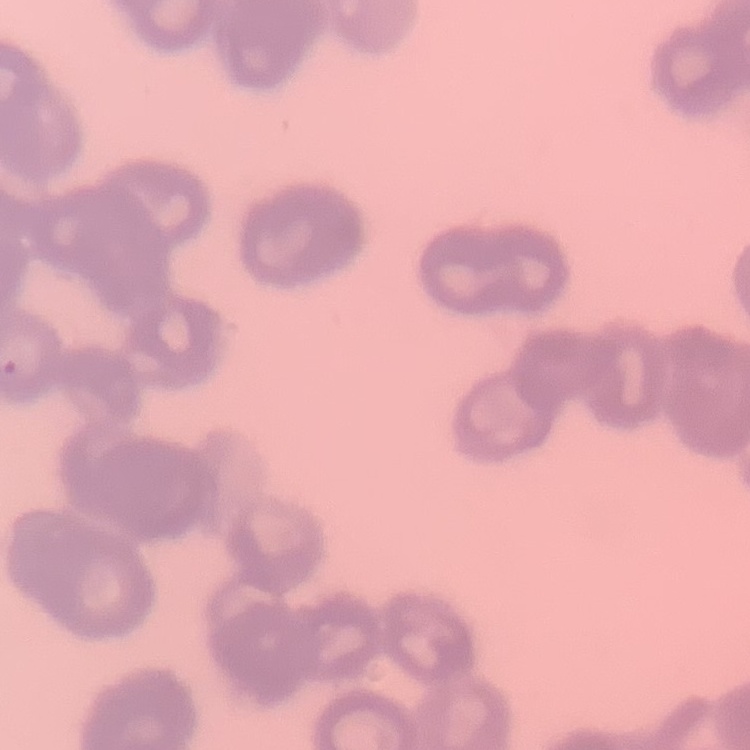

red_blood_cell_morphology: rouleaux formation
preparation: thin peripheral smear
image_type: square crop of a larger photomicrograph
stain: Field's or Giemsa